Locate every Plasmodium parasite.
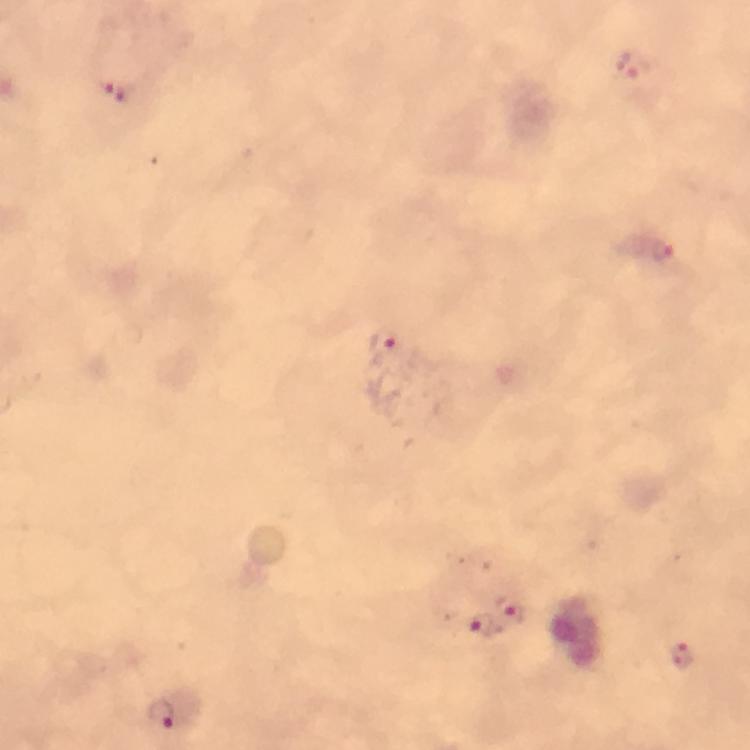

Approximate centers as {x, y} in pixels.
Plasmodium parasites: {631, 66}, {117, 90}, {663, 251}, {386, 341}, {512, 610}, {479, 626}, {681, 655}, {162, 715}.

Summary:
  - Cropped from: a single field of view
  - Capture: smartphone photograph through a microscope
  - Image size: 750×750 pixels
  - Immersion oil: applied
  - Preparation: thick blood smear
  - Context: from a malaria diagnostic workup
  - Stain: Giemsa
  - Magnification: 100x